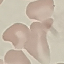

malaria status = uninfected
stain = Giemsa
capture = smartphone through the microscope eyepiece
preparation = thin blood film
image type = cell patch, automatically extracted from a larger field of view and resized to 64 × 64 pixels